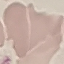

result = no malaria parasites seen
image type = cell patch, automatically extracted from a larger field of view and resized to 64 × 64 pixels
preparation = thin blood smear
capture = smartphone camera at the microscope eyepiece
stain = Giemsa